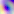
modality = micrograph
magnification = 400x
identification = Toxoplasma gondii